Identify the blood parasite species.
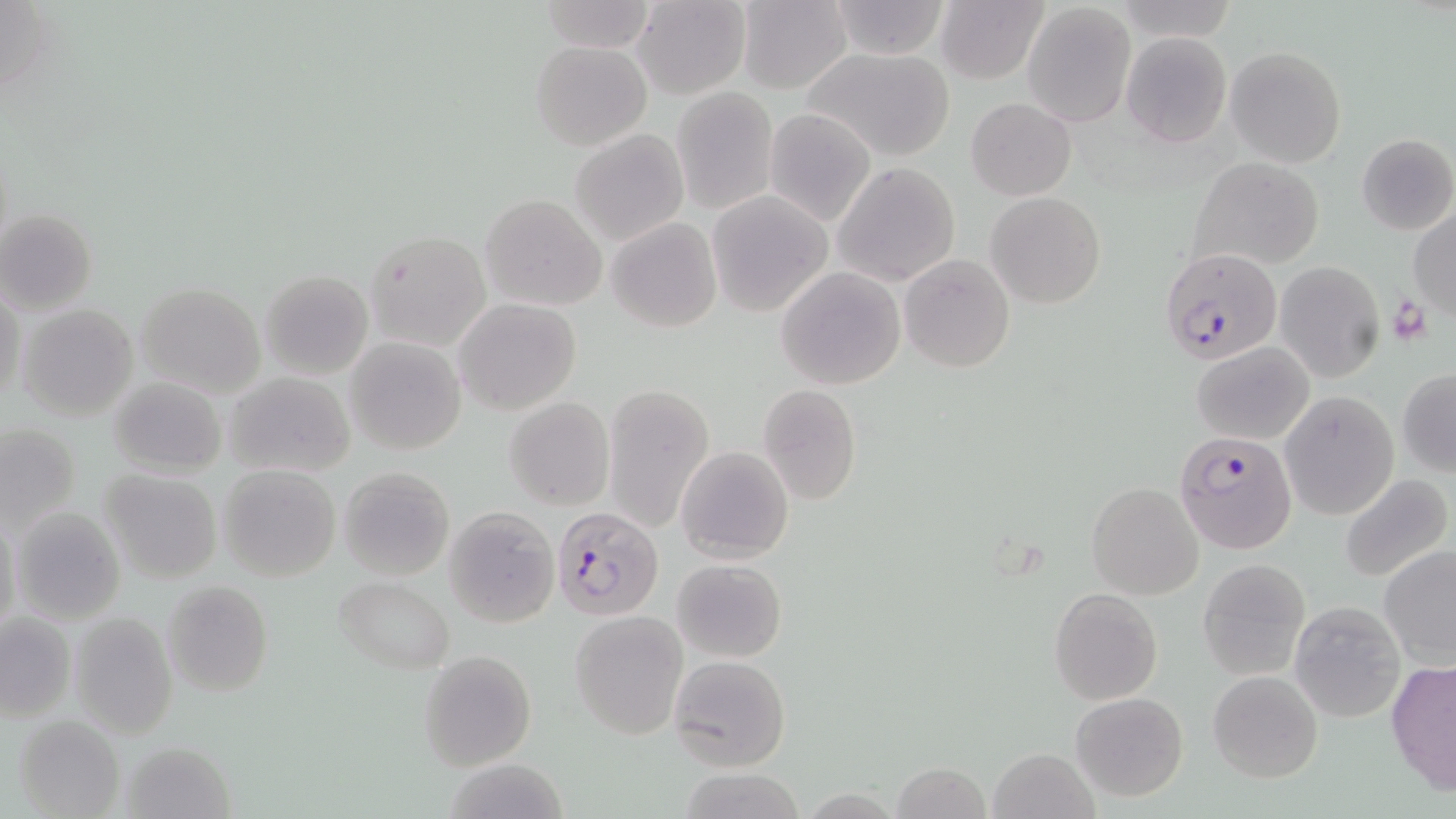
Plasmodium falciparum.

uninfected red blood cell locations = approximate bounding boxes as [x1, y1, x2, y2] in pixels: [632, 0, 749, 99], [736, 0, 854, 93], [827, 0, 953, 59], [538, 1, 655, 52], [936, 1, 1047, 84], [1114, 1, 1237, 45], [1022, 3, 1136, 126], [1121, 33, 1231, 147], [530, 40, 653, 153], [801, 45, 957, 162], [1226, 45, 1347, 167], [671, 87, 778, 214], [966, 97, 1077, 201], [764, 108, 878, 228], [569, 128, 689, 247], [1356, 133, 1456, 236], [1188, 157, 1324, 273], [834, 163, 960, 287], [706, 190, 833, 317], [986, 192, 1106, 308], [481, 193, 605, 311], [1407, 208, 1456, 319], [0, 210, 98, 314], [606, 218, 722, 332], [363, 229, 488, 350], [900, 255, 1015, 372], [1274, 261, 1385, 384], [776, 266, 907, 390], [260, 270, 372, 378], [135, 281, 265, 397], [0, 289, 23, 409], [454, 299, 582, 417], [16, 302, 140, 422], [345, 337, 467, 455], [1194, 342, 1314, 444], [1397, 369, 1456, 476], [224, 372, 356, 478], [107, 376, 226, 479], [601, 381, 717, 533], [758, 385, 862, 504], [1280, 391, 1397, 520], [504, 397, 614, 510], [1, 423, 79, 534], [677, 446, 793, 562], [218, 465, 340, 582], [338, 466, 454, 581], [99, 469, 222, 583], [1338, 473, 1453, 586], [1086, 482, 1203, 600], [11, 506, 126, 624], [444, 507, 558, 627], [1, 516, 22, 637], [1379, 544, 1456, 668], [673, 558, 786, 662], [1196, 558, 1310, 681], [334, 578, 454, 672], [162, 580, 273, 698], [1048, 587, 1162, 706], [1289, 600, 1407, 721], [0, 611, 76, 724], [570, 612, 686, 739], [68, 614, 176, 738], [419, 650, 537, 772], [668, 654, 790, 773], [1386, 661, 1456, 795], [1207, 669, 1323, 783], [1071, 692, 1188, 803], [13, 716, 124, 818], [118, 741, 233, 818], [989, 746, 1099, 818], [891, 763, 992, 819], [679, 770, 807, 818]
Plasmodium falciparum-infected red blood cell locations = approximate bounding boxes as [x1, y1, x2, y2] in pixels: [1161, 247, 1282, 365], [1174, 429, 1297, 555], [552, 506, 664, 621]
platelet locations = approximate bounding boxes as [x1, y1, x2, y2] in pixels: [1388, 297, 1430, 346]
image size = 1456×819 pixels
modality = light microscopy
stain = May-Grünwald-Giemsa
magnification = 1000x
preparation = thin blood smear
field of view = one of a larger specimen